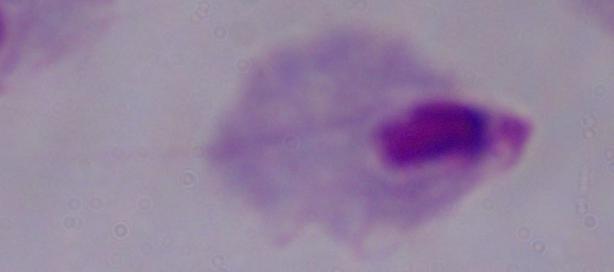
modality = photomicrograph
magnification = 1000x
identification = trichomonad